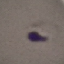

Result: malaria parasites identified. Giemsa stain. Automatically extracted cell patch, resized to 64 × 64 pixels. Acquired by smartphone through the microscope eyepiece. Thin blood film.